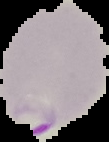
Image is 109×142 pixels. Cell region segmented out of the field of view; the surrounding area is masked to black. From a thin blood smear. Malaria status: parasitized.